Assess this cell for malaria.
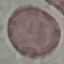
It is uninfected.

Thin blood film. Automatically extracted cell patch, resized to 64 × 64 pixels. Giemsa stain. Acquired by smartphone through the microscope eyepiece.